Identify the parasite.
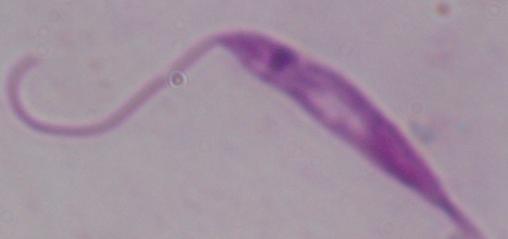

Leishmania.

{
  "magnification": "1000x",
  "modality": "photomicrograph"
}